Identify the parasite.
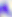
This is Toxoplasma gondii.

modality = photomicrograph
magnification = 400x